Classify this cell by malaria status.
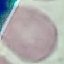
It is uninfected.

Giemsa-stained preparation. Thin smear of blood. Photographed with a smartphone camera at the microscope eyepiece. Automatically extracted cell patch, resized to 64 × 64 pixels.